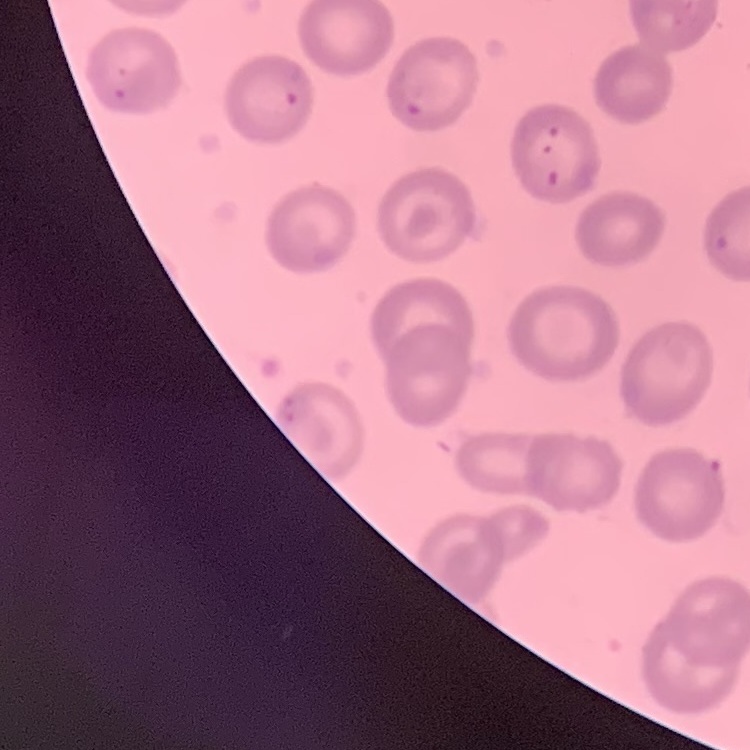
erythrocyte morphology = no rouleaux formation
stain = Field's or Giemsa
image type = one tile cut from a larger photomicrograph
preparation = thin peripheral smear